Assess this cell for malaria.
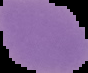
It is uninfected.

image type = cell region segmented out of the field of view; surrounding area masked to black
image size = 88×73 pixels
preparation = thin blood smear